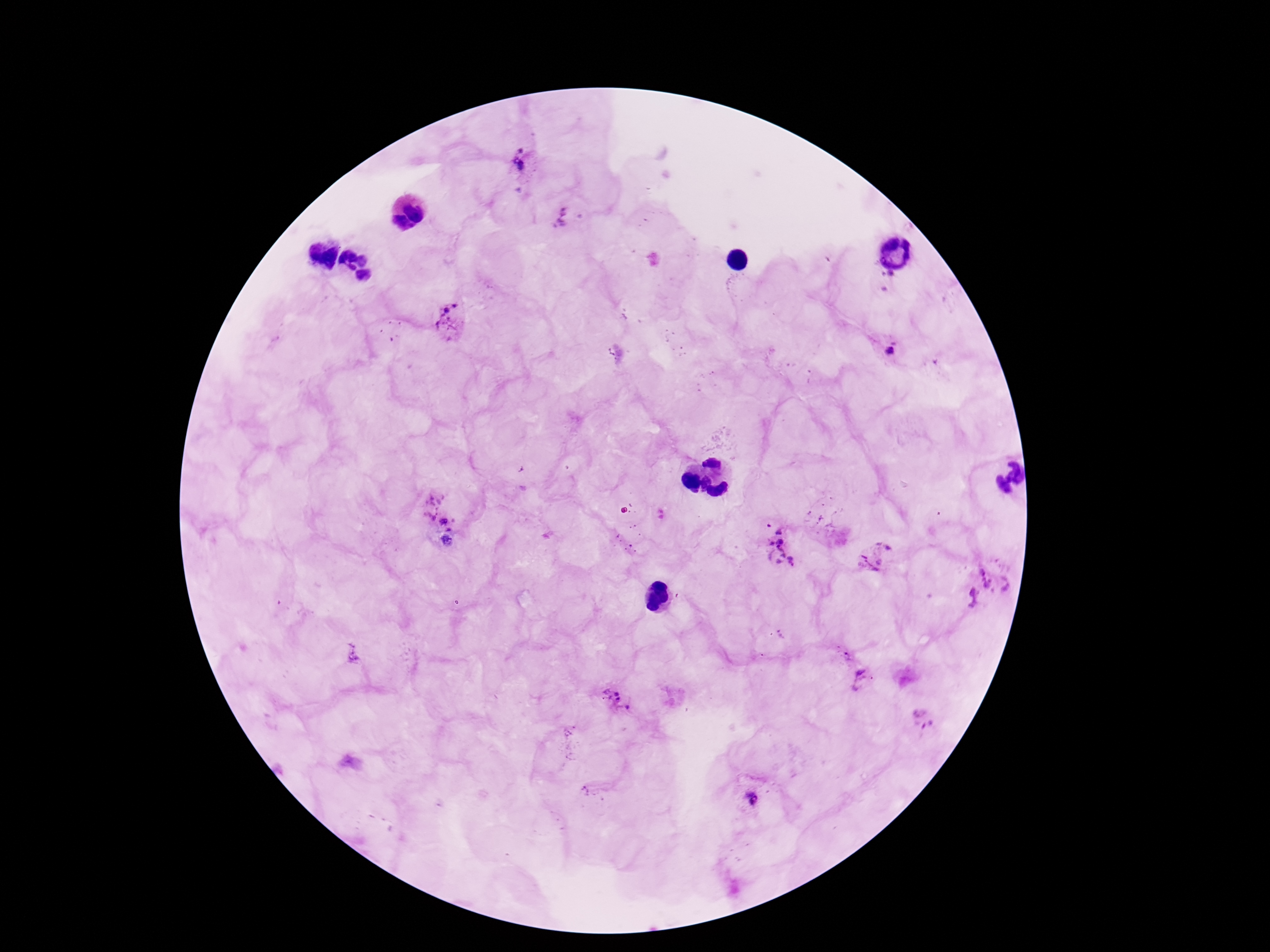

field_of_view: one from this slide
stain: Giemsa
plasmodium_parasite_locations: 'approximate centers as (x, y) in pixels: (518, 167), (565, 222), (448, 323), (888, 349), (437, 509), (771, 524), (447, 543), (875, 553), (781, 554), (997, 579), (966, 601), (842, 653), (863, 680), (615, 700), (922, 719), (752, 799)'
capture: smartphone camera through the microscope eyepiece
magnification: 100x
image_size: 1270×952 pixels
patient_malaria_status: positive
preparation: thick blood film